Assess the morphology of the red blood cells.
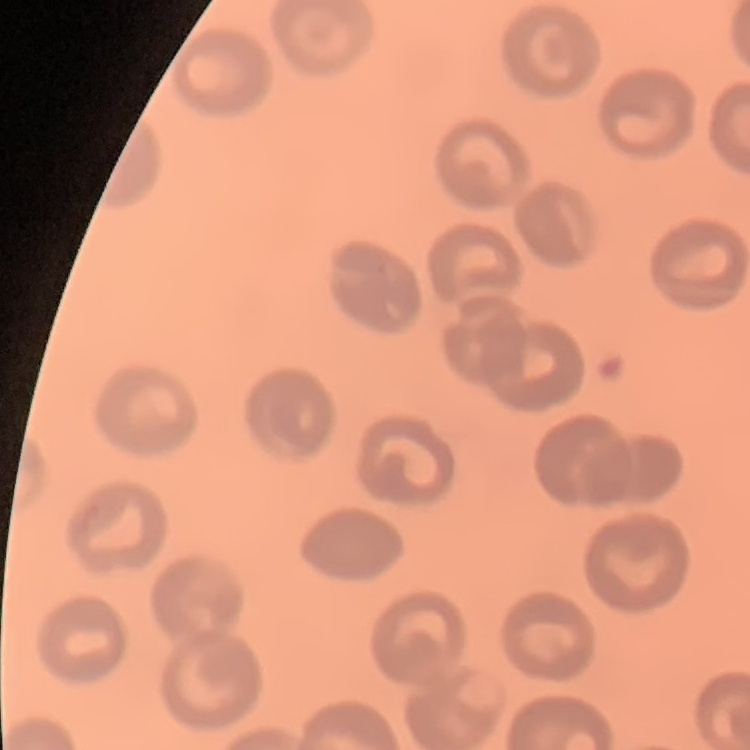
No rouleaux formation.

stain: Field's or Giemsa
image_type: one tile cut from a larger photomicrograph
preparation: thin blood film